Comment on the morphology of the erythrocytes.
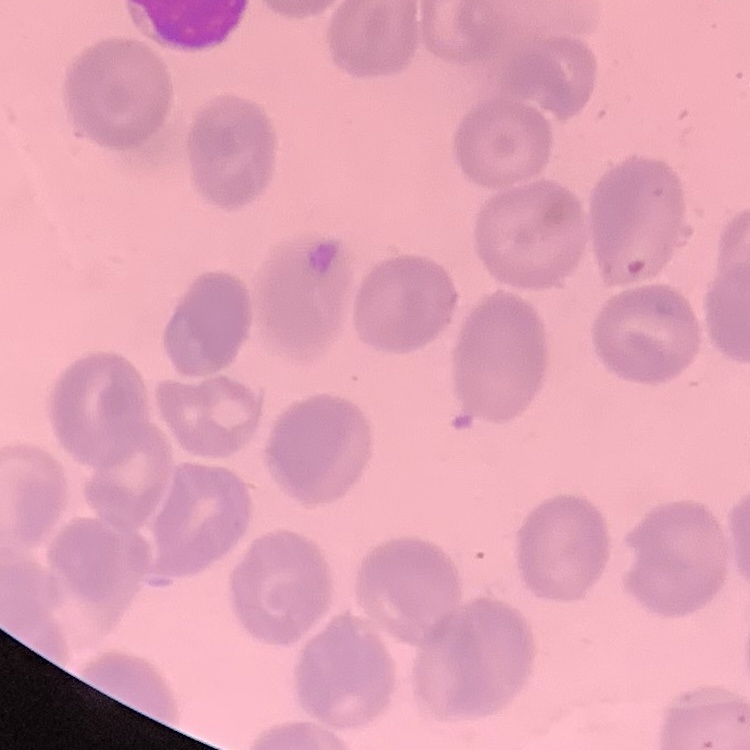

They show no rouleaux formation.

Thin blood film. Square crop of a larger photomicrograph. Field's or Giemsa stain.